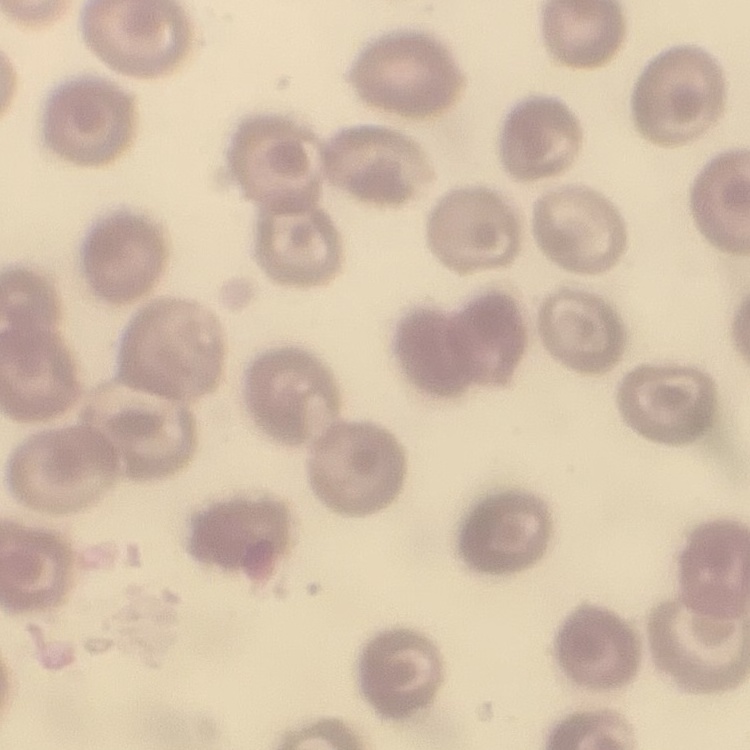
{
  "red_blood_cell_morphology": "no rouleaux formation",
  "preparation": "thin blood film",
  "image_type": "one tile cut from a larger photomicrograph",
  "stain": "Field's or Giemsa"
}